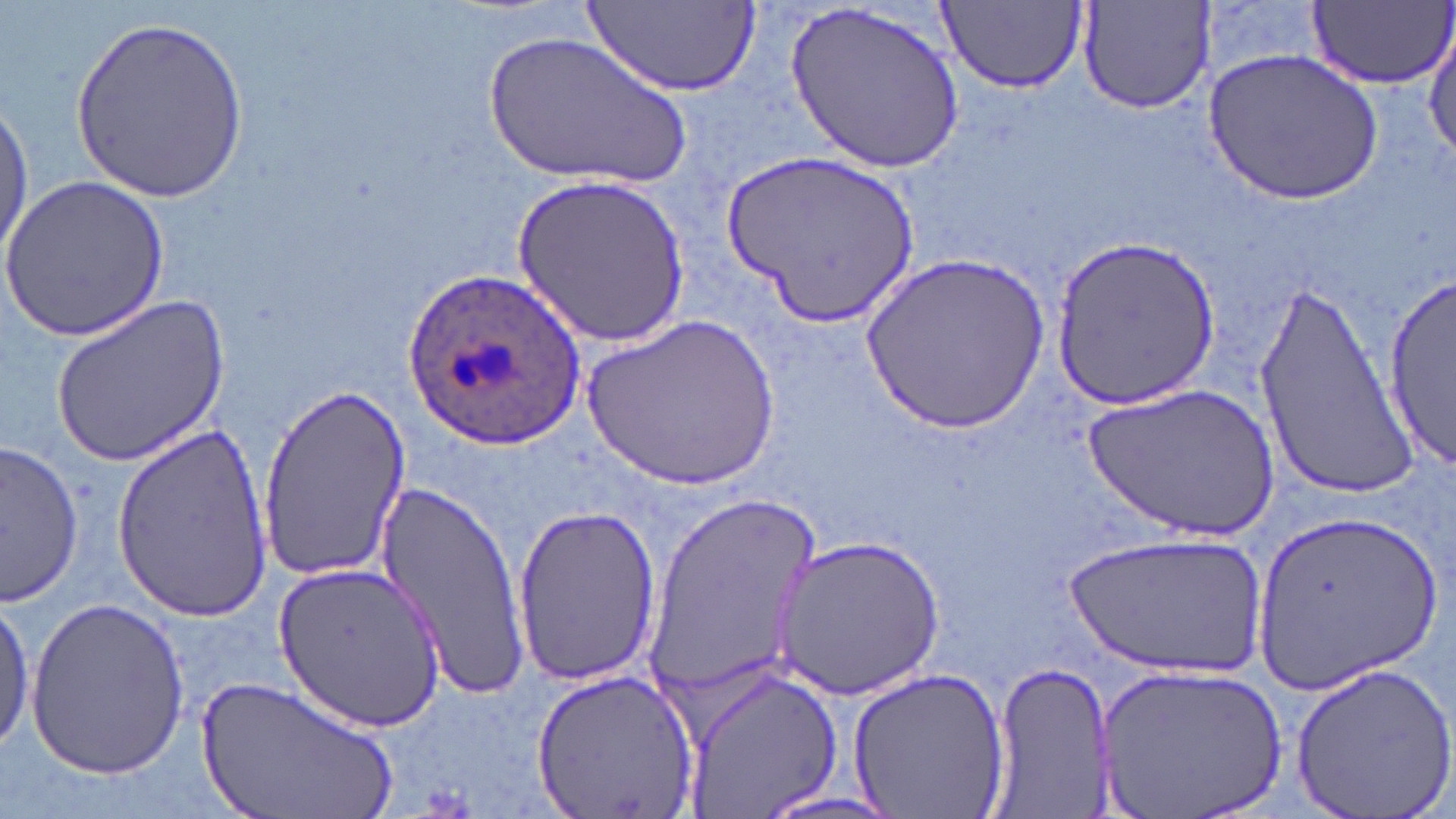 Approximate bounding boxes as (x1,y1)-(x2,y2) corner pairs in pixels. Plasmodium ovale-infected red blood cell locations: (403,267)-(588,450). Uninfected red blood cell locations: (1305,0)-(1453,88), (939,1)-(1087,92), (1077,1)-(1217,117), (585,2)-(759,98), (785,4)-(964,173), (70,13)-(247,200), (1425,24)-(1456,165), (481,28)-(692,192), (1206,50)-(1381,204), (0,100)-(35,262), (718,149)-(917,329), (1,173)-(173,341), (514,176)-(689,348), (1052,234)-(1220,411), (864,252)-(1049,432), (1374,265)-(1455,480), (1254,276)-(1424,497), (52,294)-(233,465), (582,313)-(781,491), (258,382)-(411,581), (1081,383)-(1281,540), (112,421)-(272,623), (3,440)-(83,606), (367,479)-(530,695), (642,492)-(820,706), (512,503)-(665,686), (1250,505)-(1442,693), (1065,535)-(1265,673), (773,536)-(946,700), (274,561)-(445,734), (25,594)-(191,781), (0,599)-(36,755), (987,660)-(1116,816), (1291,660)-(1456,813), (1097,662)-(1286,818), (528,664)-(698,818), (683,665)-(842,818), (846,666)-(1011,817), (198,674)-(401,819), (751,793)-(912,818). Slide-level diagnosis: Plasmodium ovale. Light microscopy. Captured at 1000x magnification. Image is 1456×819 pixels. Single field of view. May-Grünwald-Giemsa-stained preparation. Thin blood smear.